Assess this cell for malaria.
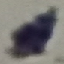
It is uninfected.

{
  "capture": "smartphone through the microscope eyepiece",
  "stain": "Giemsa",
  "image_type": "cell patch, automatically extracted from a larger field of view and resized to 64 × 64 pixels",
  "preparation": "thin blood film"
}